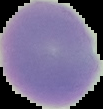
Summary:
  - Preparation: thin blood smear
  - Image size: 103×109 pixels
  - Malaria status: uninfected
  - Image type: cell region segmented out of the field of view; surrounding area masked to black